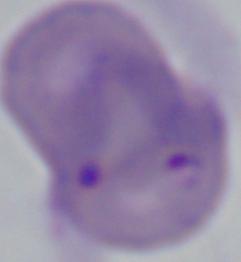
{
  "magnification": "1000x",
  "modality": "micrograph",
  "identification": "Babesia"
}